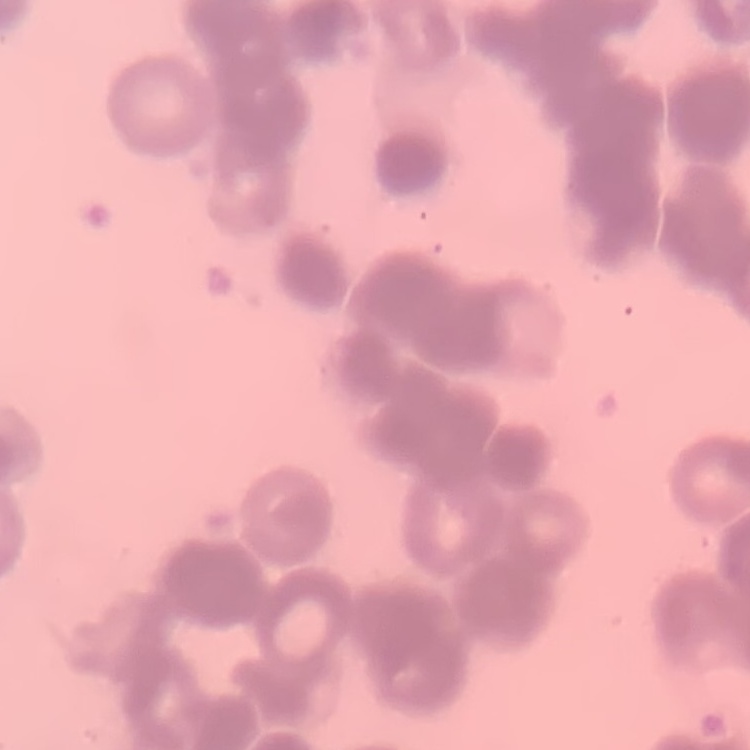
erythrocyte morphology = rouleaux formation
preparation = thin blood film
stain = Field's or Giemsa
image type = square crop of a larger photomicrograph